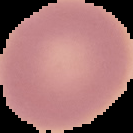

{
  "result": "no Plasmodium parasites seen",
  "image_type": "segmented cell region on a black background",
  "preparation": "thin blood smear",
  "image_size": "133×133 pixels"
}